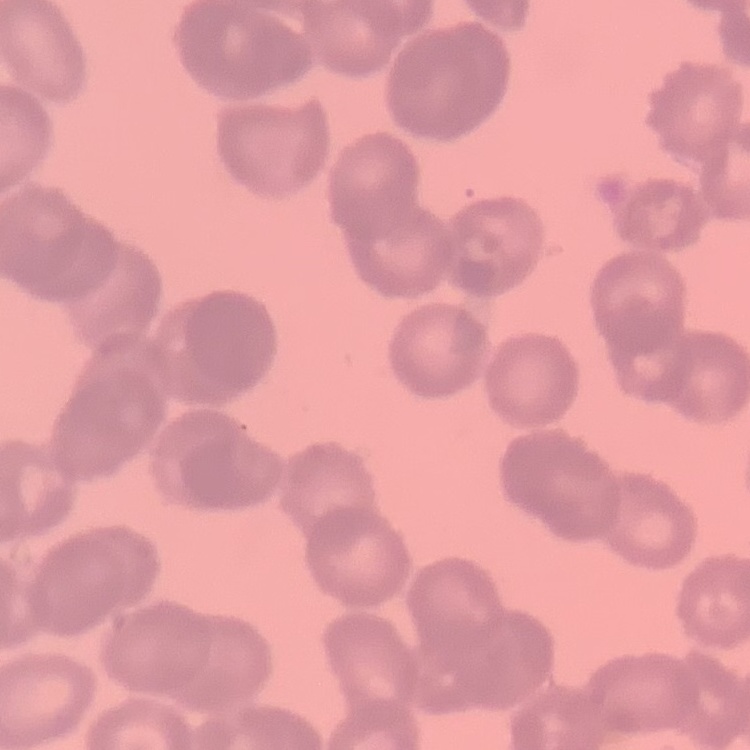

Summary:
  - Red blood cell morphology: rouleaux formation
  - Preparation: thin peripheral smear
  - Image type: square crop of a larger photomicrograph
  - Stain: Field's or Giemsa